Look for Plasmodium parasites.
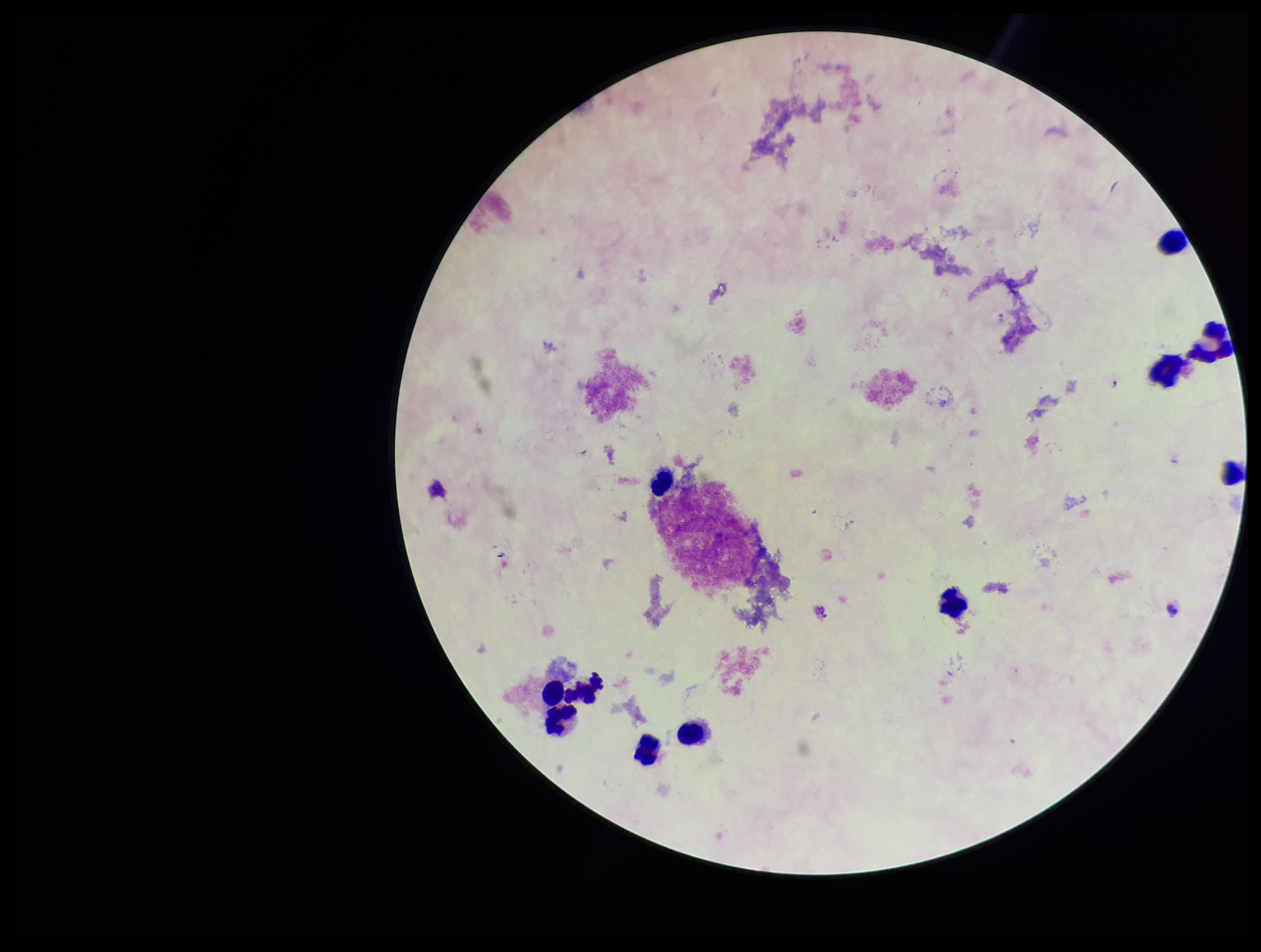
Seen.

leukocyte count = 11
patient malaria status = infected
image size = 1261×952 pixels
capture = smartphone photograph through the microscope eyepiece
preparation = thick blood smear
parasite count = 1
stain = Giemsa
field of view = single
species reported for this patient = Plasmodium falciparum